Classify this cell by malaria status.
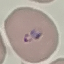

Parasitized.

Summary:
  - Capture: smartphone camera at the microscope eyepiece
  - Image type: cell patch, automatically extracted from a larger field of view and resized to 64 × 64 pixels
  - Stain: Giemsa
  - Preparation: thin blood smear